Point out every Plasmodium parasite.
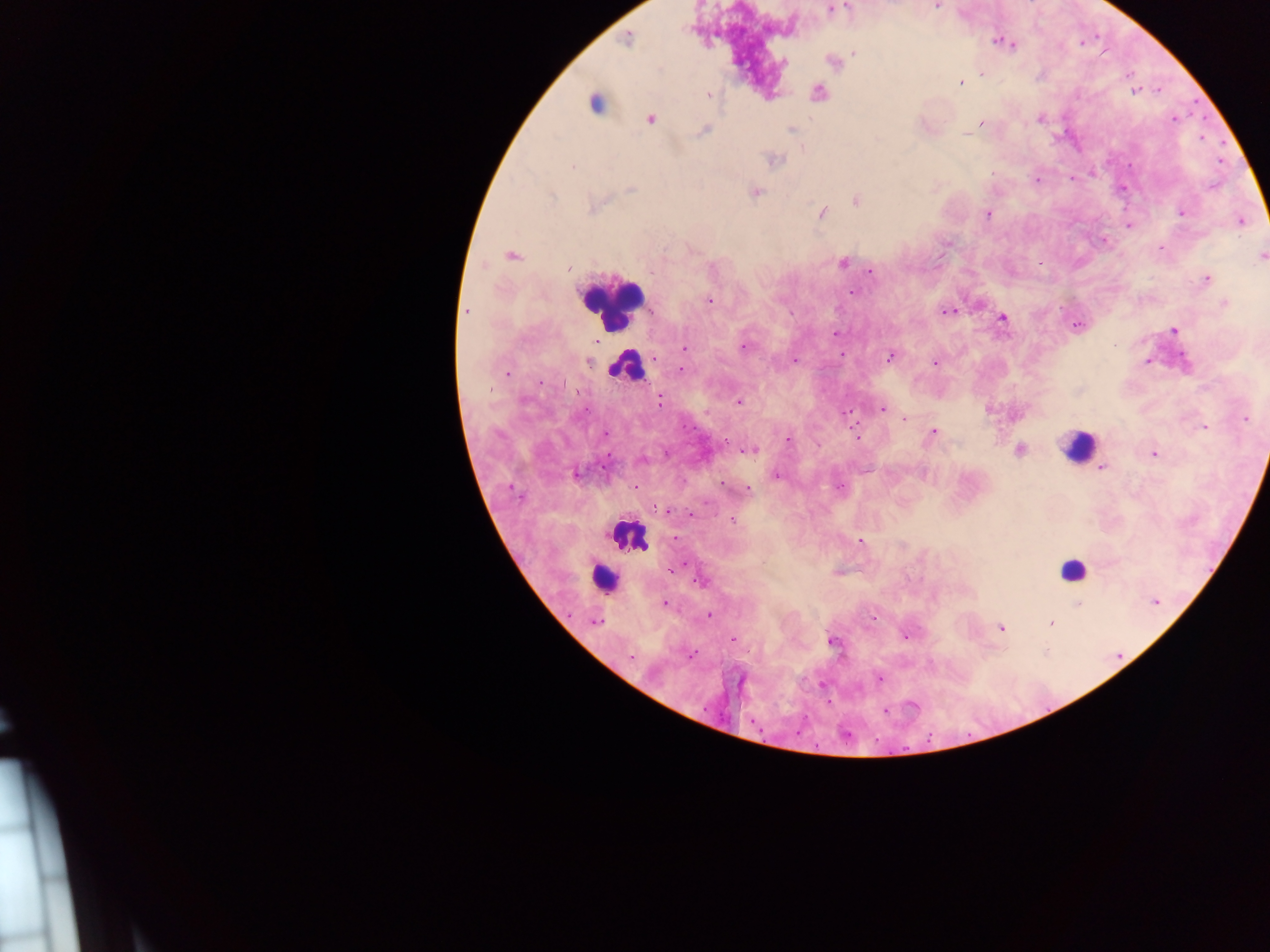
Approximate centers as x y in pixels.
Plasmodium parasites: 830 10; 627 39; 1000 42; 1009 43; 854 54; 982 73; 960 82; 818 92; 1135 92; 709 95; 650 119; 1040 119; 981 123; 791 129; 703 130; 966 134; 775 160; 572 166; 1037 180; 631 189; 757 193; 856 200; 823 213; 1182 213; 987 214; 1243 221; 1129 225; 511 256; 1261 256; 842 263; 568 269; 870 271; 1206 279; 853 292; 709 301; 1224 304; 466 311; 948 311; 1002 318; 1078 326; 1173 330; 836 333; 744 347; 684 348; 841 354; 890 357; 654 358; 794 360; 1147 361; 588 363; 935 363; 682 371; 508 373; 659 402; 738 402; 882 409; 847 413; 905 419; 1245 419; 1203 427; 934 431; 604 434; 857 437; 788 439; 1020 450; 750 451; 1154 453; 642 460; 1102 467; 577 474; 777 475; 748 490; 664 511; 733 520; 860 541; 674 570; 702 582; 1155 602; 665 604; 1078 604; 708 616; 594 622; 1051 624; 1001 627; 906 636; 733 640; 831 641; 630 657; 879 679; 886 710.

{
  "country": "Ghana",
  "image_size": "1270×952 pixels",
  "preparation": "thick blood film",
  "leukocyte_locations": "approximate centers as x y in pixels: 594 103; 612 304; 623 364; 1078 446; 626 536; 1072 568; 599 571",
  "capture": "mobile-phone photograph through a microscope",
  "field_of_view": "single"
}